Point out each Plasmodium parasite.
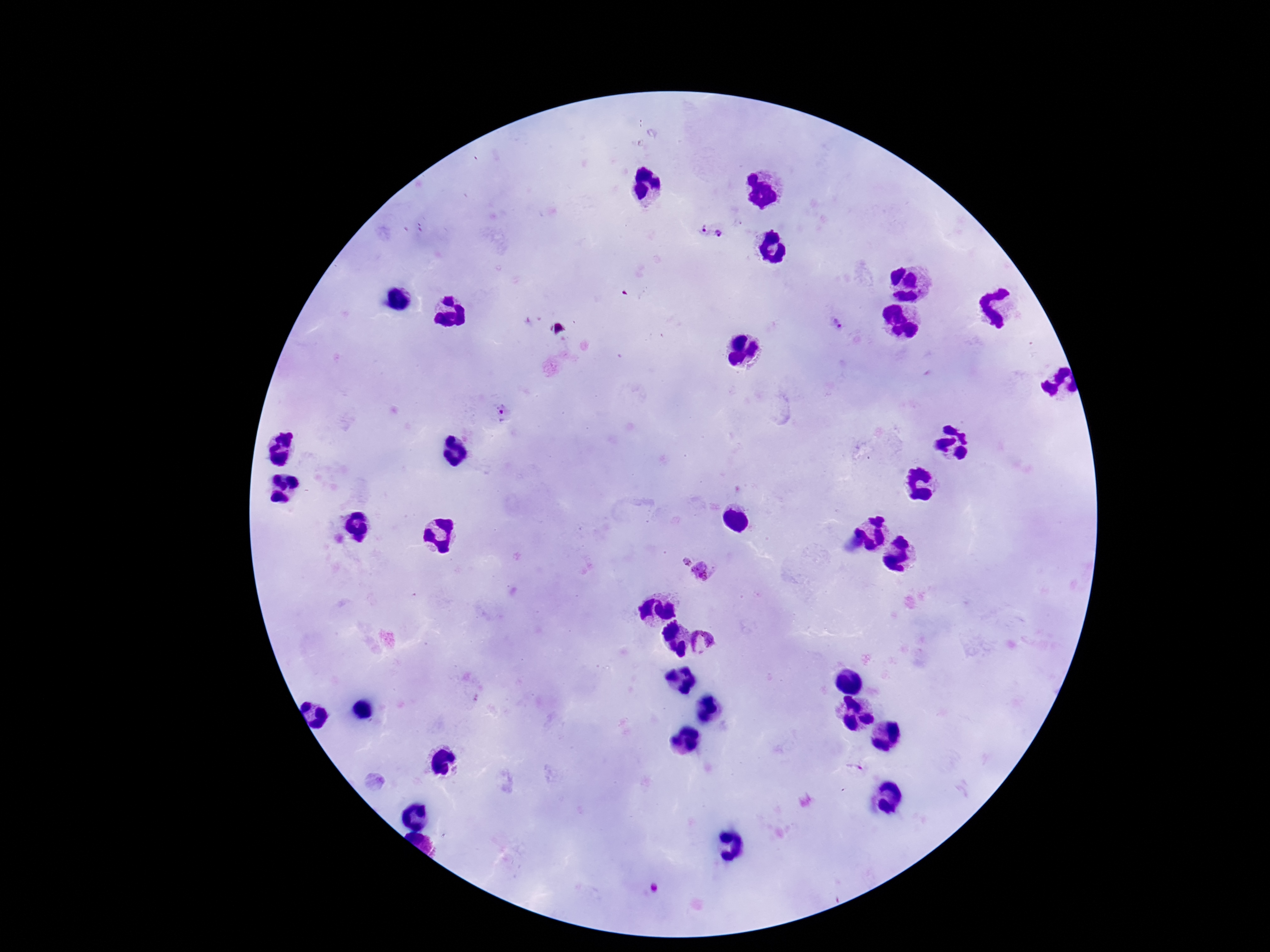

Approximate centers as [x, y] in pixels.
Plasmodium parasites: [703, 230], [719, 230], [838, 325], [505, 411], [685, 562], [702, 570], [705, 641].

Thick blood smear. Single field of view. Patient malaria status: positive. Image is 1270×952 pixels. Giemsa stain. Smartphone photograph taken through the microscope eyepiece. 100x magnification.